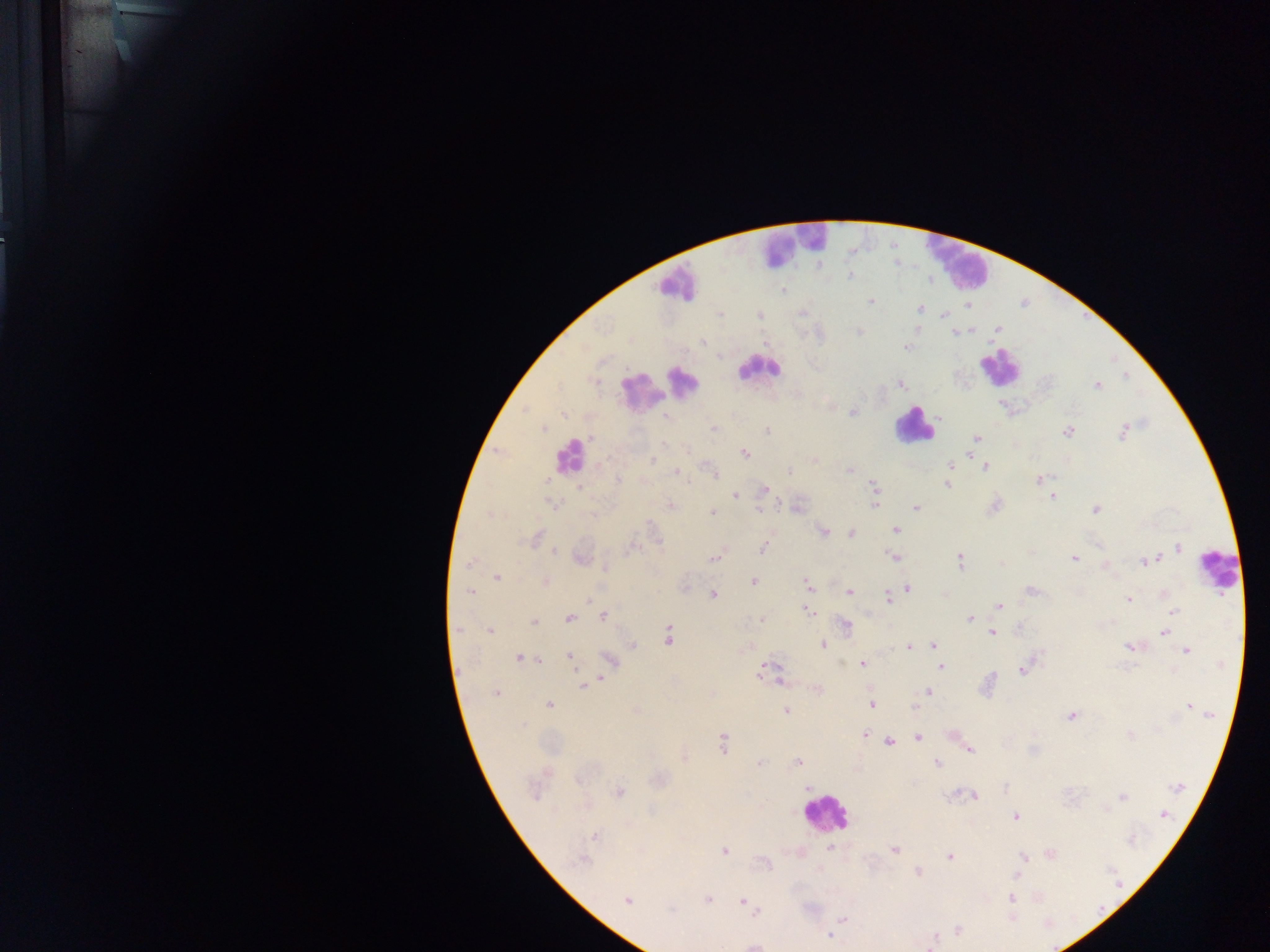 Approximate centers as (x, y) in pixels. Leukocyte locations: (795, 245), (956, 256), (675, 283), (756, 368), (1000, 371), (686, 382), (643, 398), (914, 425), (573, 458), (1222, 576), (824, 816). Malaria parasite locations: (852, 277), (781, 291), (870, 301), (920, 308), (719, 314), (758, 315), (945, 316), (942, 317), (995, 330), (859, 331), (973, 331), (954, 336), (702, 342), (603, 357), (776, 371), (1124, 376), (1126, 379), (901, 384), (1099, 386), (853, 412), (564, 413), (664, 417), (713, 427), (542, 428), (767, 430), (1069, 431), (1122, 433), (591, 437), (976, 438), (663, 443), (687, 449), (745, 453), (652, 462), (950, 465), (986, 466), (850, 470), (678, 471), (789, 471), (713, 473), (549, 479), (616, 480), (686, 480), (1039, 480), (873, 483), (948, 485), (764, 488), (579, 489), (735, 496), (1053, 496), (876, 498), (544, 500), (554, 504), (671, 504), (781, 505), (916, 509), (758, 510), (1095, 510), (711, 512), (489, 514), (647, 525), (895, 529), (824, 532), (852, 533), (535, 539), (1179, 547), (762, 549), (554, 552), (715, 558), (895, 558), (1074, 560), (1150, 560), (472, 561), (960, 561), (1144, 562), (469, 564), (1001, 564), (605, 569), (495, 578), (753, 581), (546, 582), (807, 586), (910, 587), (1031, 589), (809, 590), (469, 591), (849, 593), (712, 594), (887, 598), (1129, 599), (590, 600), (999, 606), (807, 611), (1173, 612), (604, 616), (569, 618), (970, 618), (762, 620), (534, 624), (845, 624), (487, 630), (846, 630), (459, 631), (992, 631), (1165, 631), (490, 632), (669, 637), (821, 645), (631, 646), (933, 646), (1128, 646), (936, 647), (907, 648), (1186, 651), (569, 656), (518, 658), (540, 662), (862, 662), (840, 663), (573, 666), (764, 666), (941, 667), (1021, 671), (760, 672), (1016, 673), (601, 678), (781, 682), (583, 688), (929, 691), (496, 694), (870, 704), (548, 706), (1188, 706), (913, 709), (786, 710), (1208, 714), (1070, 716), (865, 734), (1130, 736), (918, 738), (889, 742), (723, 746), (971, 751), (797, 761), (759, 763), (936, 763), (1179, 787), (621, 790), (807, 790), (952, 793), (975, 797), (1123, 797), (1105, 810), (1165, 815), (1015, 816), (593, 836), (829, 849), (896, 849), (724, 851), (1051, 855), (949, 856), (1023, 857), (581, 860), (766, 865), (917, 873), (1017, 876), (627, 899), (707, 899), (1012, 899), (741, 900), (669, 911), (757, 911), (1012, 916), (843, 919), (959, 928), (829, 935), (933, 940). Sample from Ghana. Image is 1270×952 pixels. Photographed through a microscope with a mobile-phone camera. Thick blood smear. Single field of view.